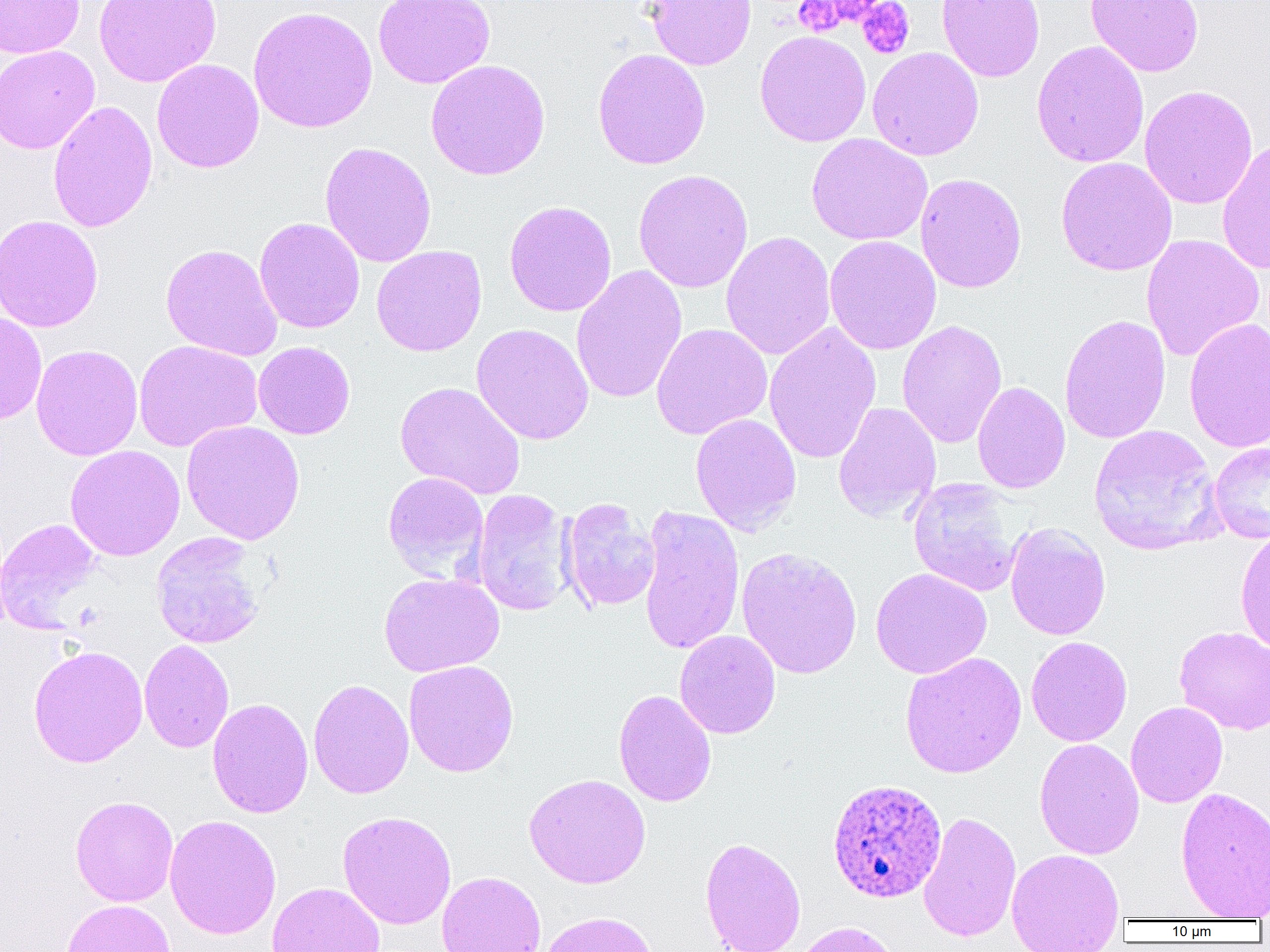

slide_level_diagnosis: Plasmodium ovale
image_size: 1270×952 pixels
platelet_locations: 'approximate bounding boxes as (x1,y1)-(x2,y2) corner pairs in pixels: (793,0)-(849,36), (857,1)-(914,59)'
modality: optical microscopy
uninfected_red_blood_cell_locations: 'approximate bounding boxes as (x1,y1)-(x2,y2) corner pairs in pixels: (0,0)-(84,58), (93,0)-(221,87), (373,0)-(495,89), (644,0)-(757,70), (936,0)-(1045,82), (1085,0)-(1205,77), (248,5)-(378,133), (754,30)-(871,147), (1031,40)-(1150,168), (0,45)-(100,154), (867,47)-(984,160), (592,48)-(711,170), (152,59)-(264,173), (425,59)-(550,181), (1139,84)-(1258,209), (48,100)-(158,233), (806,133)-(932,246), (1217,138)-(1270,274), (319,141)-(437,267), (1055,157)-(1177,276), (632,169)-(754,293), (915,173)-(1027,293), (504,200)-(617,317), (0,215)-(103,332), (254,217)-(365,333), (720,230)-(836,361), (1141,233)-(1264,362), (824,235)-(942,355), (160,243)-(283,360), (371,245)-(487,357), (570,264)-(688,405), (0,310)-(47,425), (1058,314)-(1171,444), (1183,317)-(1270,454), (897,320)-(1007,449), (763,321)-(882,464), (471,323)-(594,446), (651,323)-(772,440), (134,339)-(263,452), (253,341)-(355,439), (31,344)-(143,461), (395,381)-(526,500), (972,381)-(1071,494), (833,402)-(941,523), (690,413)-(802,535), (181,420)-(305,544), (1088,424)-(1223,555), (1209,443)-(1270,544), (65,445)-(185,561), (383,471)-(489,582), (907,477)-(1024,597), (471,489)-(575,616), (560,497)-(660,613), (637,504)-(745,656), (0,517)-(103,633), (1004,522)-(1111,641), (1235,528)-(1270,654), (150,532)-(267,649), (736,546)-(862,680), (870,567)-(992,679), (378,572)-(504,677), (1174,626)-(1270,735), (674,629)-(781,739), (1026,636)-(1132,747), (139,639)-(234,753), (27,645)-(148,768), (899,651)-(1027,779), (403,660)-(519,777), (308,678)-(414,799), (613,689)-(716,807), (208,698)-(313,818), (1126,701)-(1228,808), (1034,738)-(1145,860), (524,773)-(650,889), (1175,786)-(1270,920), (70,796)-(179,906), (336,810)-(457,930), (918,811)-(1021,942), (164,814)-(281,939), (699,836)-(806,952), (1006,848)-(1125,952), (436,871)-(546,952), (267,882)-(386,952), (62,899)-(177,952), (539,911)-(659,952), (790,920)-(900,952)'
plasmodium_ovale_infected_red_blood_cell_locations: 'approximate bounding boxes as (x1,y1)-(x2,y2) corner pairs in pixels: (827,777)-(946,903)'
preparation: thin blood film
magnification: 1000x
field_of_view: single